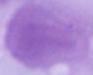 1000x magnification. A red blood cell is seen. Micrograph.